Point out each Plasmodium parasite.
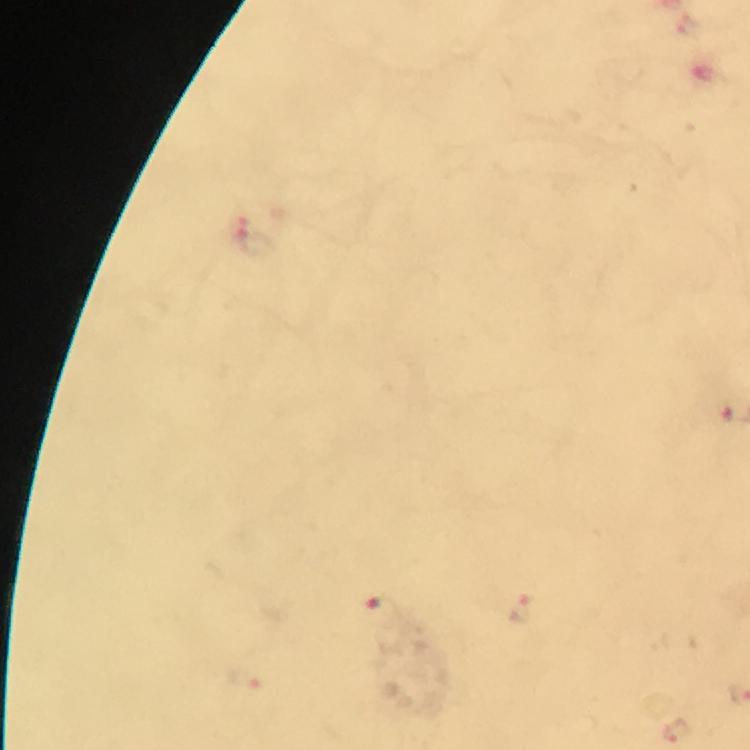

Approximate centers as (x, y) in pixels.
Plasmodium parasites: (256, 241), (522, 609), (382, 610), (675, 730).

Summary:
  - Preparation: thick blood film
  - Image size: 750×750 pixels
  - Magnification: 100x
  - Cropped from: one field of view
  - Context: from a diagnostic examination for malaria
  - Capture: smartphone photograph through a microscope
  - Immersion oil: used
  - Stain: Giemsa